Point out each Plasmodium parasite and classify it by life-cycle stage.
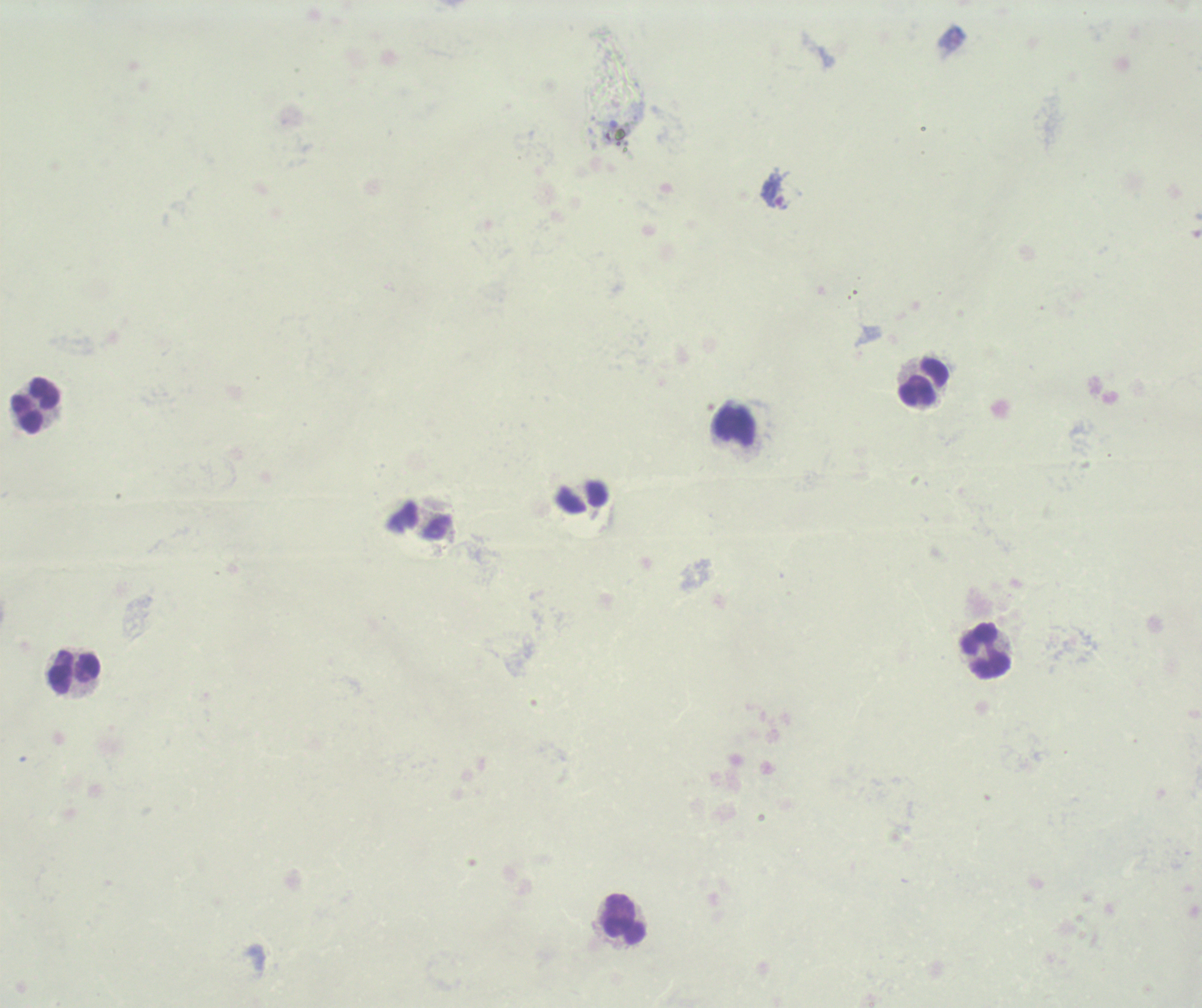

Approximate centers as (x, y) in pixels.
Trophozoites: (775, 189).
No schizont or gametocyte forms observed.

Approximate centers as (x, y) in pixels.
Summary:
  - Leukocyte locations: (923, 380), (35, 405), (734, 426), (985, 651), (73, 673), (624, 919)
  - Field of view: one from this slide
  - Image size: 1202×1008 pixels
  - Stain: Romanowsky
  - Context: previously used in a real diagnosis
  - Preparation: thick blood film
  - Background quality: poor
  - Magnification: 100x